Assess this cell for malaria.
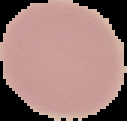
Uninfected.

Image is 127×121 pixels. Cell region segmented out of the field of view; the surrounding area is masked to black. From a thin blood smear.